Identify the blood parasite species.
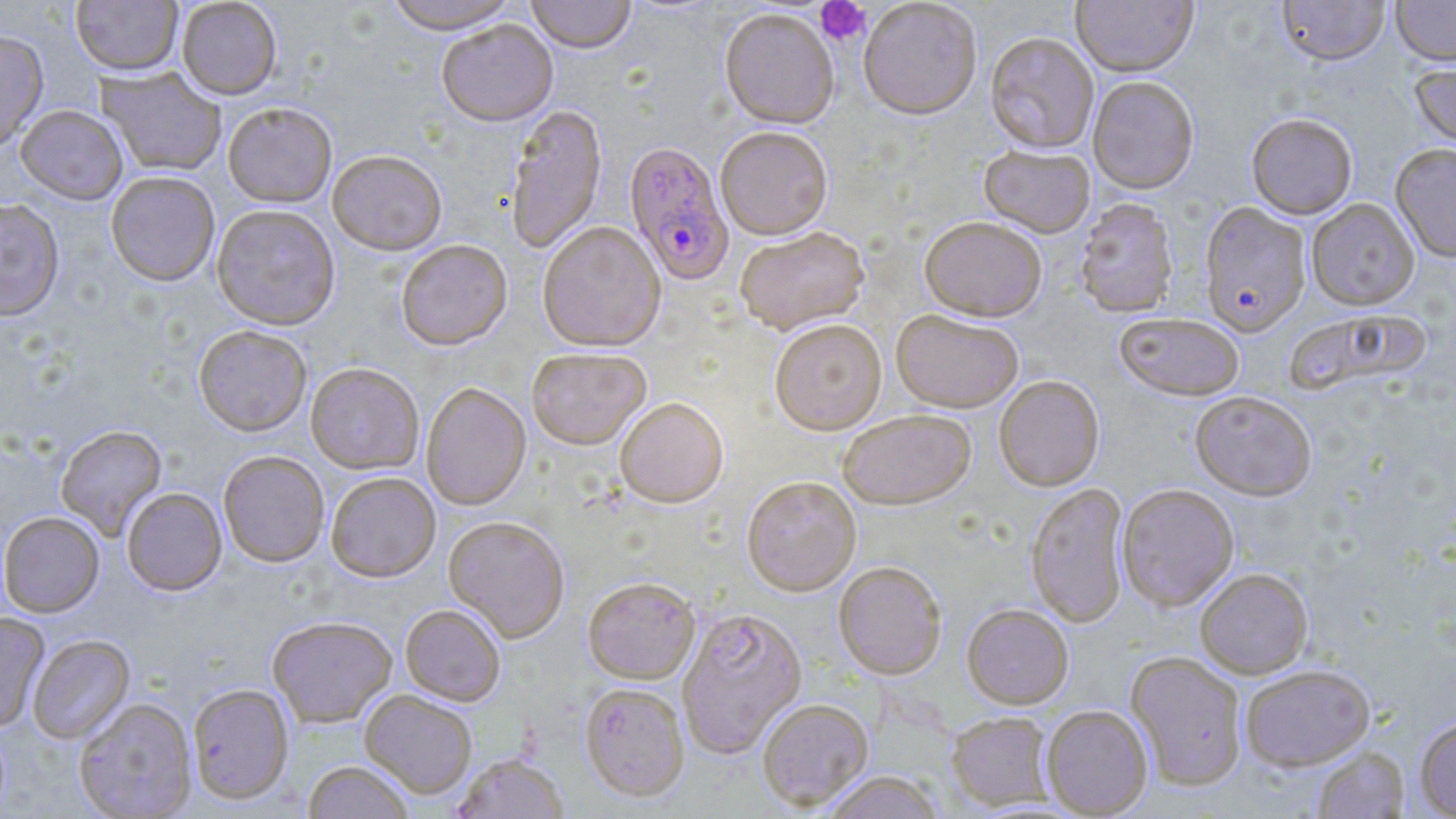

Plasmodium falciparum.

stain = May-Grünwald-Giemsa
modality = optical microscopy
preparation = thin blood film
magnification = 1000x
platelet locations = approximate bounding boxes as (x1,y1)-(x2,y2) corner pairs in pixels: (815,0)-(871,47)
uninfected red blood cell locations = approximate bounding boxes as (x1,y1)-(x2,y2) corner pairs in pixels: (70,0)-(182,76), (176,0)-(282,100), (383,0)-(521,34), (525,0)-(637,54), (1277,0)-(1390,67), (1390,0)-(1456,67), (858,1)-(982,121), (1070,1)-(1198,79), (719,10)-(840,130), (437,20)-(558,127), (0,29)-(49,154), (984,33)-(1099,155), (1409,61)-(1456,153), (96,67)-(228,177), (1088,77)-(1199,196), (223,102)-(337,208), (15,105)-(128,204), (505,105)-(607,255), (1246,115)-(1358,220), (715,128)-(833,241), (1390,144)-(1456,263), (979,146)-(1096,239), (327,152)-(447,257), (105,172)-(220,287), (0,197)-(65,321), (1075,199)-(1178,319), (1306,199)-(1419,311), (1199,202)-(1311,338), (212,205)-(340,331), (919,218)-(1046,323), (538,223)-(666,352), (735,228)-(869,336), (396,241)-(512,352), (891,310)-(1024,414), (1286,310)-(1432,399), (1114,313)-(1245,402), (770,320)-(887,435), (193,326)-(312,438), (526,349)-(652,452), (306,364)-(424,476), (994,377)-(1105,491), (421,383)-(532,511), (1190,392)-(1316,502), (614,399)-(728,509), (837,411)-(976,512), (55,425)-(168,540), (218,452)-(329,568), (326,473)-(440,583), (741,478)-(861,596), (1026,483)-(1130,628), (1117,484)-(1239,611), (121,488)-(227,597), (0,512)-(104,618), (443,516)-(570,644), (833,564)-(947,680), (1195,569)-(1313,679), (582,579)-(700,686), (962,604)-(1074,709), (400,605)-(505,707), (677,610)-(807,759), (0,613)-(50,733), (267,617)-(397,728), (28,635)-(135,745), (1126,652)-(1246,791), (1239,665)-(1375,771), (187,684)-(294,806), (580,685)-(690,804), (360,690)-(477,800), (74,699)-(198,818), (758,700)-(873,812), (1042,705)-(1153,817), (946,712)-(1055,811), (1415,717)-(1456,818), (1312,746)-(1409,818), (452,754)-(569,819), (301,762)-(415,819), (822,772)-(943,819)
Plasmodium falciparum-infected red blood cell locations = approximate bounding boxes as (x1,y1)-(x2,y2) corner pairs in pixels: (624,143)-(734,286)
field of view = one of a larger specimen
image size = 1456×819 pixels